Locate every Plasmodium parasite.
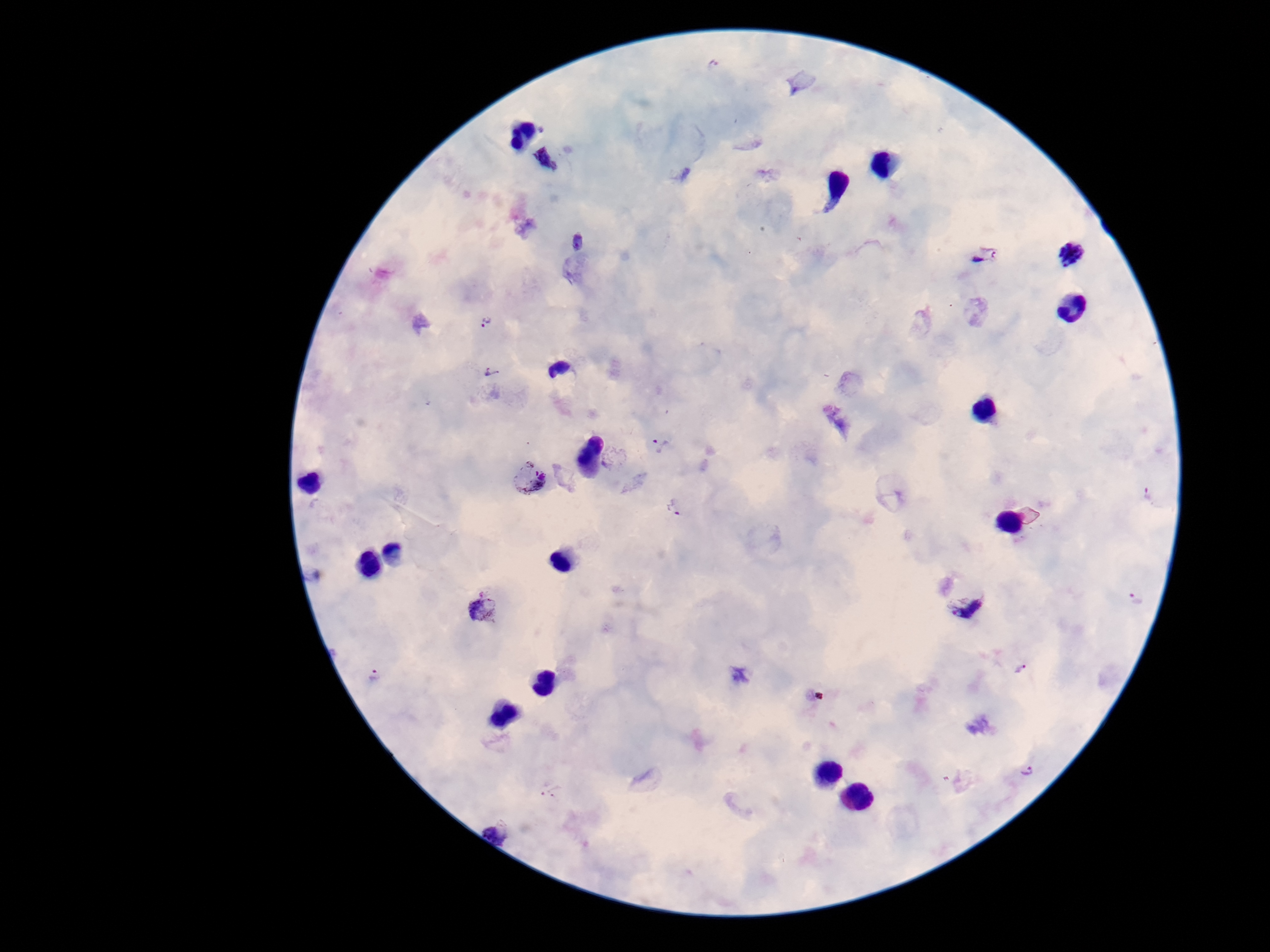

Approximate centers as {x, y} in pixels.
Plasmodium parasites: {546, 161}, {579, 243}, {1071, 254}, {985, 255}, {488, 322}, {490, 373}, {838, 420}, {661, 445}, {615, 456}, {530, 477}, {1152, 496}, {674, 508}, {1138, 598}, {963, 601}, {484, 605}, {1020, 669}, {374, 677}, {1026, 771}.

Summary:
  - Patient malaria status: infected
  - Preparation: thick blood smear
  - Image size: 1270×952 pixels
  - Magnification: 100x
  - Field of view: one from this slide
  - Capture: smartphone camera through the microscope eyepiece
  - Stain: Giemsa